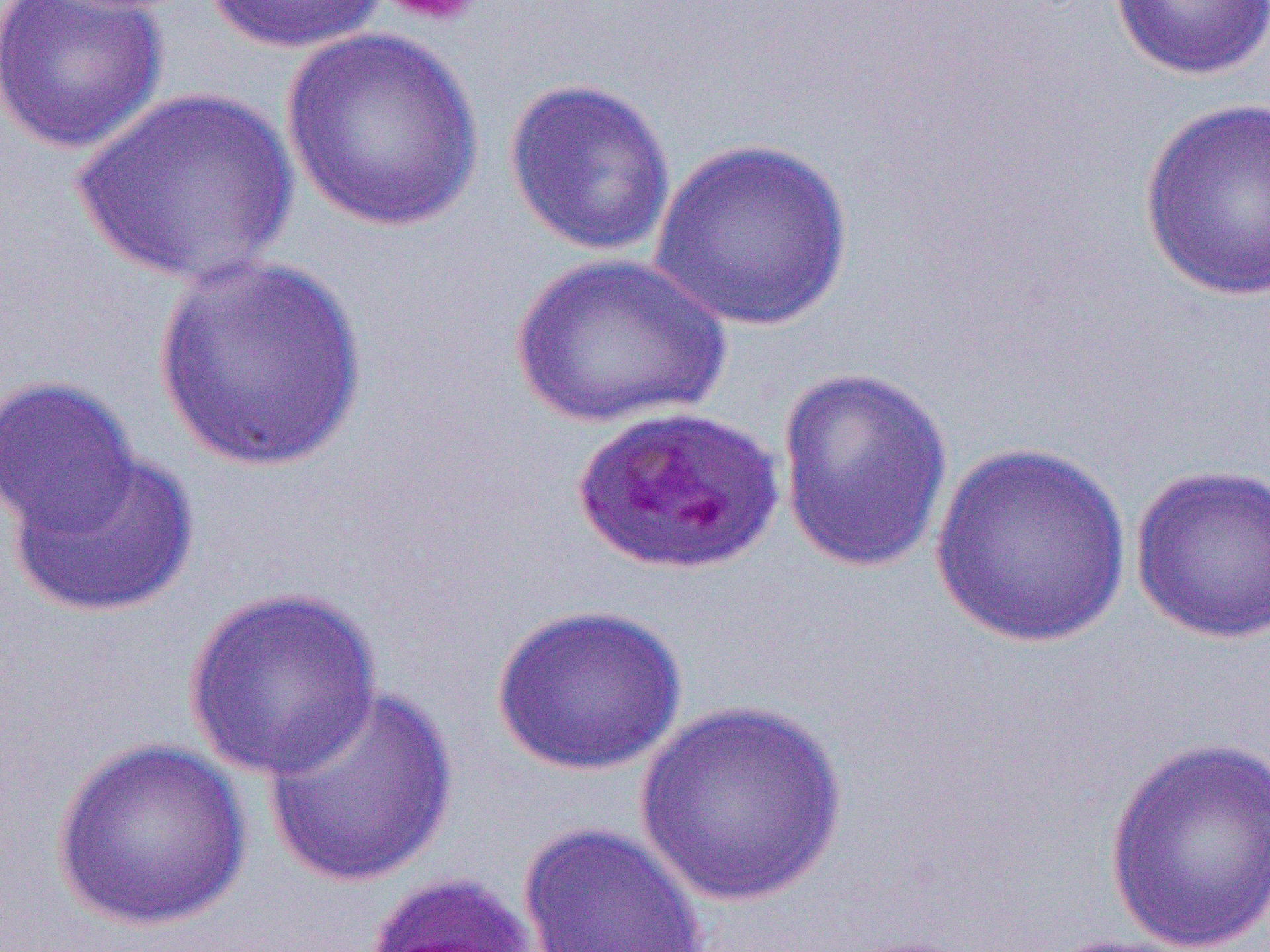

Summary:
  - Coordinate format: approximate bounding boxes as [x1, y1, x2, y2] in pixels
  - Uninfected red blood cell locations: [0, 0, 168, 155], [203, 0, 390, 55], [1108, 0, 1270, 82], [280, 28, 487, 233], [504, 76, 677, 257], [69, 87, 299, 288], [1139, 97, 1270, 303], [648, 137, 856, 332], [510, 252, 730, 429], [150, 254, 370, 474], [775, 365, 954, 574], [0, 375, 143, 541], [928, 442, 1133, 649], [9, 449, 199, 621], [1130, 463, 1269, 644], [182, 585, 383, 781], [491, 603, 688, 776], [262, 685, 459, 890], [631, 700, 849, 907], [1104, 733, 1270, 952], [51, 738, 252, 932], [517, 821, 709, 952], [1037, 932, 1209, 952]
  - Platelet locations: [376, 0, 484, 28]
  - Slide-level diagnosis: Plasmodium falciparum
  - Preparation: thin blood film
  - Image size: 1270×952 pixels
  - Field of view: one of a larger specimen
  - Magnification: 1000x
  - Modality: light microscopy